Describe the morphology of the red blood cells.
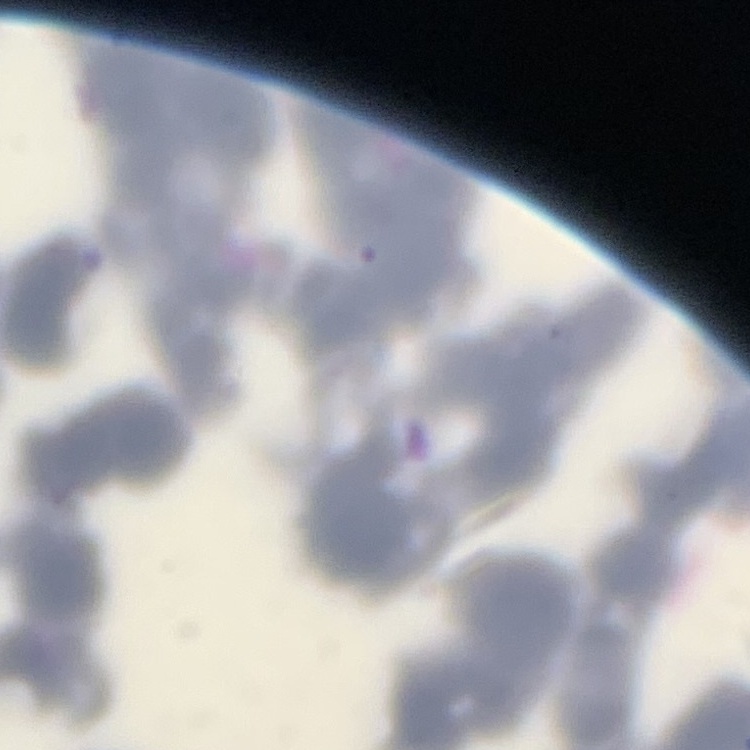
Rouleaux formation.

Thin peripheral smear. Square crop of a larger photomicrograph. Stained with either Field's or Giemsa.